Locate and identify every blood parasite.
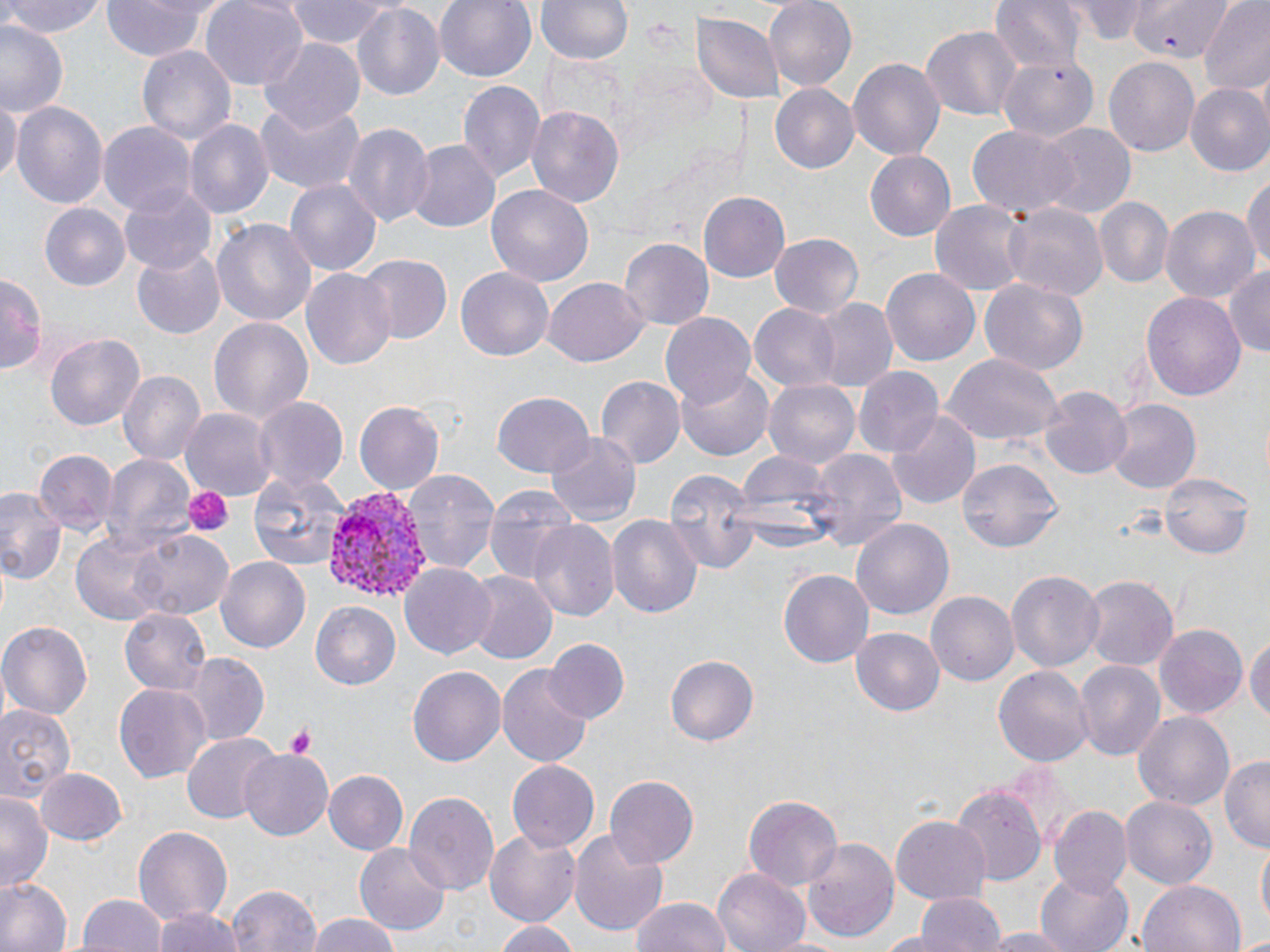
Approximate bounding boxes as (x1, y1, x2, y2) in pixels.
Plasmodium vivax-infected red blood cells: (326, 490, 433, 607).
No Plasmodium falciparum, Plasmodium ovale, Plasmodium malariae, Babesia divergens, or Trypanosoma brucei observed.

slide_level_diagnosis: Plasmodium vivax
stain: May-Grünwald-Giemsa
modality: optical microscopy
platelet_locations: 'approximate bounding boxes as (x1, y1, x2, y2) in pixels: (184, 485, 233, 535), (285, 726, 315, 758)'
image_size: 1270×952 pixels
preparation: thin blood smear
field_of_view: single
uninfected_red_blood_cell_locations: 'approximate bounding boxes as (x1, y1, x2, y2) in pixels: (0, 0, 107, 40), (100, 0, 212, 63), (200, 0, 306, 88), (281, 0, 390, 48), (435, 0, 535, 83), (538, 0, 633, 66), (764, 0, 857, 90), (989, 0, 1086, 72), (1071, 0, 1153, 41), (1197, 0, 1270, 95), (354, 2, 446, 101), (2, 4, 82, 80), (694, 13, 781, 106), (0, 24, 66, 116), (922, 26, 1021, 121), (258, 37, 365, 135), (137, 42, 235, 144), (997, 56, 1098, 144), (848, 57, 945, 162), (1103, 58, 1200, 159), (456, 81, 545, 184), (769, 85, 859, 174), (1184, 85, 1270, 177), (0, 97, 20, 184), (253, 99, 366, 195), (11, 101, 108, 213), (527, 105, 624, 209), (184, 119, 275, 221), (342, 119, 435, 228), (100, 123, 196, 218), (1037, 123, 1135, 222), (966, 126, 1075, 219), (408, 140, 498, 235), (866, 152, 955, 239), (1244, 168, 1269, 277), (285, 178, 383, 277), (486, 183, 594, 288), (119, 185, 216, 276), (698, 193, 789, 281), (1093, 196, 1172, 288), (930, 199, 1025, 296), (1005, 202, 1107, 302), (43, 203, 130, 290), (1162, 203, 1260, 302), (211, 219, 317, 327), (769, 232, 864, 318), (619, 237, 715, 332), (133, 249, 225, 338), (358, 254, 452, 344), (301, 265, 397, 369), (1225, 265, 1269, 362), (454, 267, 554, 361), (881, 267, 979, 366), (0, 274, 44, 376), (543, 279, 648, 366), (981, 279, 1088, 376), (1142, 289, 1246, 403), (808, 297, 898, 393), (748, 303, 841, 391), (660, 314, 755, 410), (207, 316, 314, 424), (43, 333, 145, 431), (942, 355, 1063, 446), (854, 368, 942, 458), (119, 369, 206, 467), (677, 369, 775, 460), (596, 376, 685, 471), (764, 378, 862, 468), (1038, 385, 1133, 479), (491, 391, 596, 479), (253, 395, 349, 495), (1106, 400, 1199, 492), (354, 401, 445, 495), (182, 407, 278, 503), (888, 412, 978, 507), (548, 432, 641, 526), (36, 448, 114, 532), (809, 448, 908, 554), (732, 450, 839, 547), (102, 454, 197, 555), (958, 459, 1064, 552), (7, 465, 97, 575), (402, 468, 499, 577), (664, 468, 758, 577), (1160, 471, 1255, 560), (247, 472, 348, 569), (483, 484, 582, 582), (0, 487, 63, 588), (607, 512, 702, 624), (851, 518, 954, 620), (527, 519, 619, 624), (129, 529, 231, 621), (71, 533, 168, 624), (216, 557, 310, 654), (401, 563, 496, 662), (1006, 569, 1104, 672), (464, 571, 557, 665), (779, 571, 873, 666), (1082, 577, 1177, 670), (928, 593, 1019, 687), (310, 602, 401, 690), (120, 610, 210, 696), (0, 622, 92, 720), (1153, 623, 1248, 721), (1245, 628, 1270, 731), (850, 629, 945, 717), (543, 639, 628, 725), (184, 653, 270, 742), (665, 654, 758, 747), (1074, 660, 1165, 762), (993, 662, 1091, 766), (497, 664, 594, 769), (406, 667, 505, 767), (114, 683, 210, 784), (0, 701, 76, 808), (1132, 711, 1234, 811), (181, 733, 280, 822), (237, 746, 335, 841), (1220, 755, 1270, 853), (506, 761, 598, 852), (1004, 761, 1086, 848), (37, 767, 127, 846), (324, 772, 409, 854), (605, 775, 700, 867), (947, 784, 1040, 888), (0, 790, 52, 891), (405, 792, 498, 894), (1121, 794, 1217, 888), (743, 795, 843, 891), (1049, 806, 1131, 898), (891, 815, 991, 905), (132, 825, 233, 926), (570, 828, 669, 938), (485, 831, 579, 923), (802, 835, 899, 941), (1256, 843, 1269, 929), (354, 844, 451, 934), (712, 867, 811, 952), (1035, 870, 1134, 952), (0, 875, 73, 952), (1137, 878, 1246, 952), (227, 884, 322, 952), (910, 891, 1009, 952), (75, 893, 166, 952), (630, 896, 731, 952), (150, 906, 248, 952), (304, 913, 407, 952), (493, 919, 577, 952), (977, 929, 1077, 952), (1239, 931, 1270, 952)'
magnification: 1000x